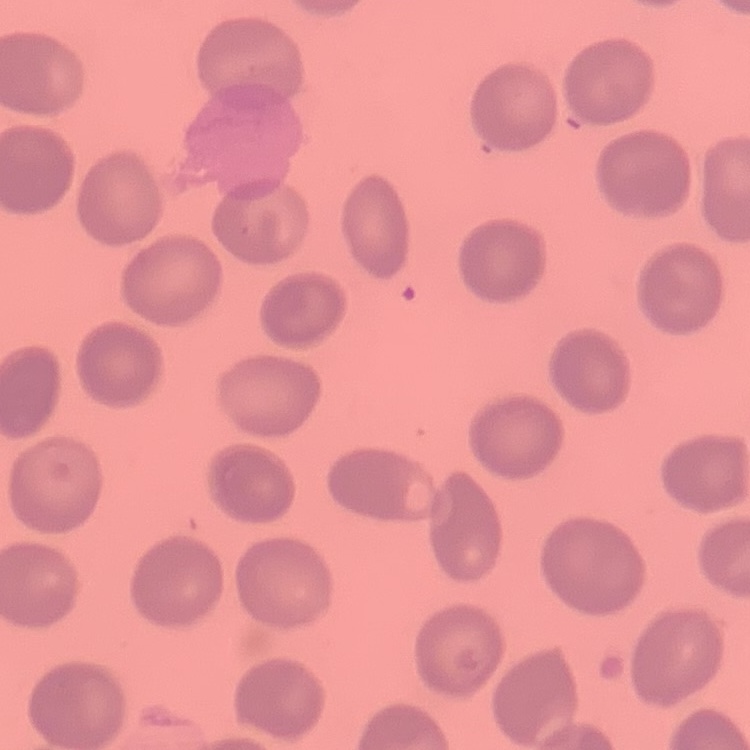
erythrocyte morphology = no rouleaux formation
preparation = thin blood smear
stain = Field's or Giemsa
image type = one tile cut from a larger photomicrograph